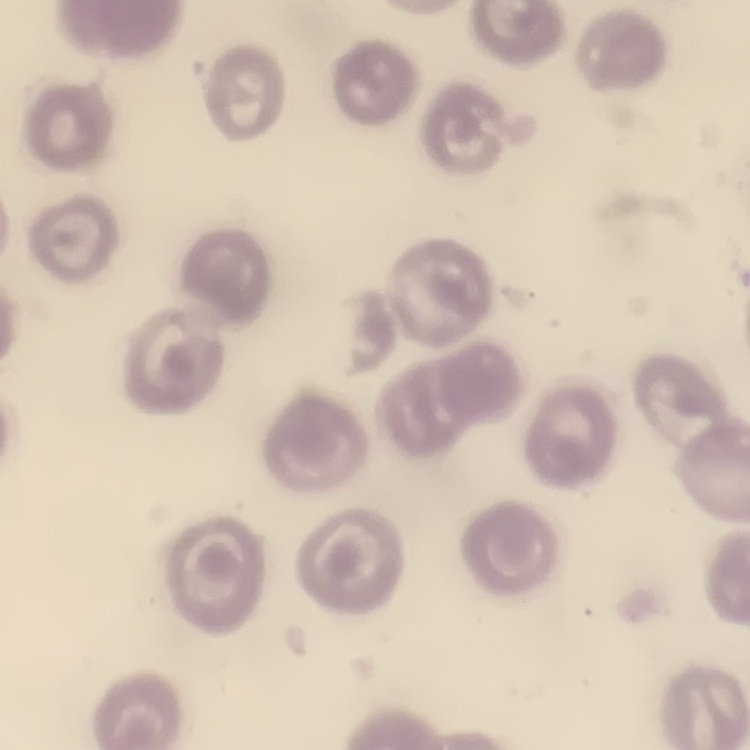

{
  "red_blood_cell_morphology": "no rouleaux formation",
  "stain": "Field's or Giemsa",
  "preparation": "thin blood film",
  "image_type": "square crop of a larger photomicrograph"
}